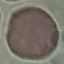 Malaria status: uninfected. Thin blood smear. Acquired by smartphone through the microscope eyepiece. Giemsa stain. Cell patch, automatically extracted from a larger field of view and resized to 64 × 64 pixels.